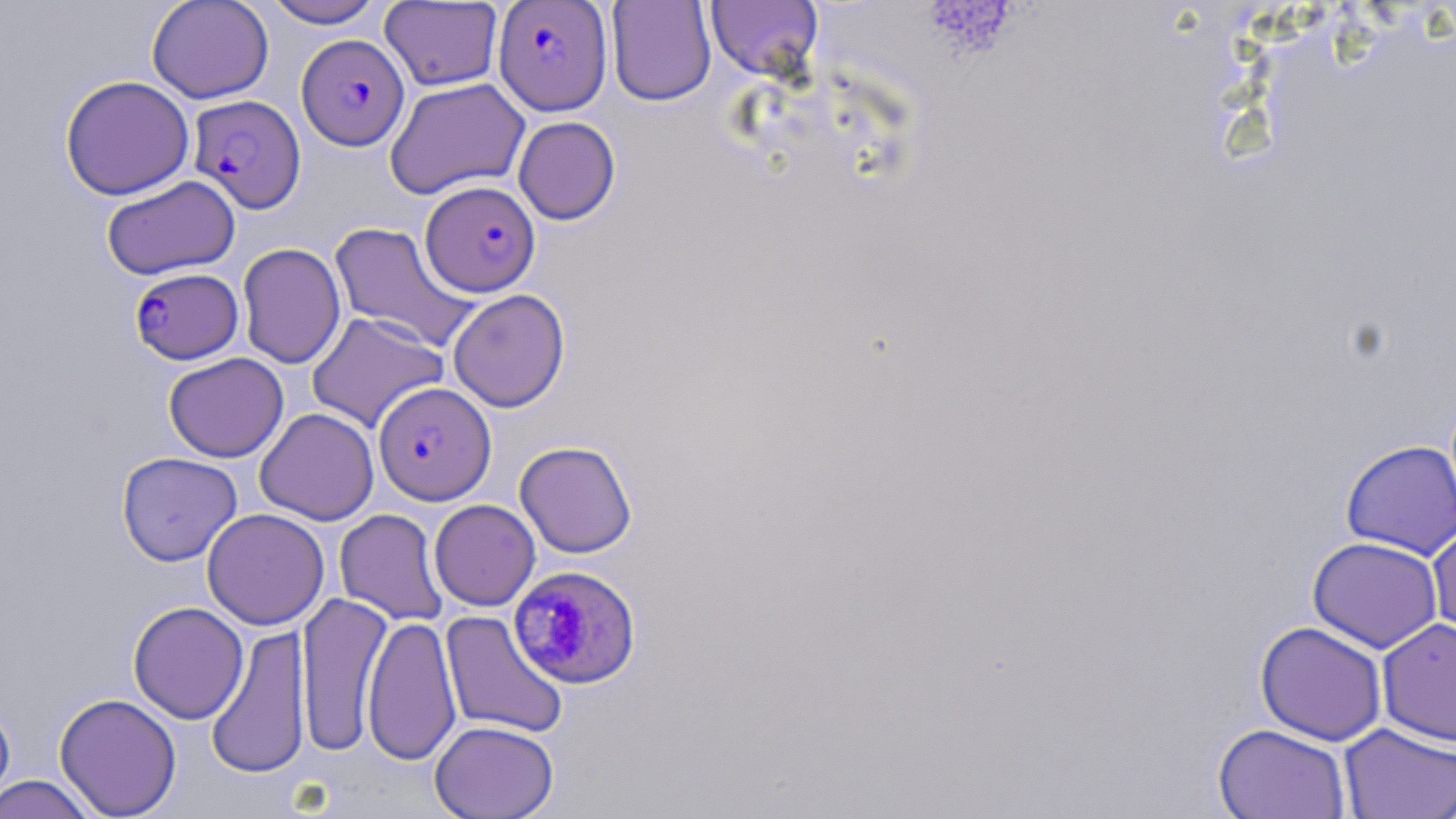

Approximate bounding boxes as (x1, y1, x2, y2) in pixels. Plasmodium falciparum-infected red blood cell locations: (493, 1, 612, 115), (297, 33, 409, 150), (188, 95, 306, 214), (421, 181, 541, 297), (129, 267, 244, 364), (373, 381, 496, 505), (508, 564, 643, 689). Uninfected red blood cell locations: (146, 0, 275, 104), (262, 0, 386, 29), (606, 0, 717, 106), (379, 1, 504, 91), (706, 1, 823, 83), (59, 75, 195, 200), (385, 78, 529, 200), (513, 116, 621, 225), (101, 175, 240, 280), (328, 221, 479, 352), (237, 242, 346, 369), (447, 289, 570, 412), (306, 311, 449, 433), (163, 352, 289, 462), (254, 408, 379, 525), (1340, 438, 1456, 560), (514, 440, 638, 558), (116, 451, 242, 566), (429, 499, 541, 611), (202, 508, 330, 630), (334, 509, 449, 626), (1426, 519, 1456, 645), (1307, 536, 1443, 653), (295, 592, 392, 756), (127, 602, 249, 724), (439, 610, 569, 740), (362, 614, 461, 766), (1377, 617, 1456, 746), (1255, 620, 1388, 745), (205, 625, 311, 780), (54, 693, 182, 817), (0, 695, 16, 812), (430, 719, 559, 819), (1212, 723, 1352, 819), (1339, 723, 1456, 818), (0, 775, 100, 819). Slide-level diagnosis: Plasmodium falciparum. Image is 1456×819 pixels. Optical microscopy. 1000x magnification. Thin blood film. One field of a larger specimen. May-Grünwald-Giemsa-stained preparation.